Name the parasite shown.
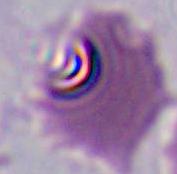
Plasmodium.

modality = micrograph
magnification = 400x or 1000x